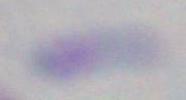

Summary:
  - Magnification: 1000x
  - Identification: Toxoplasma gondii
  - Modality: photomicrograph